Identify the cell.
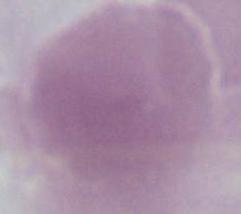
This is an erythrocyte.

{
  "magnification": "1000x",
  "modality": "micrograph"
}